Assess this cell for malaria.
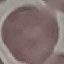

Uninfected.

Acquired by smartphone through the microscope eyepiece. Giemsa-stained preparation. Thin blood film. Cell patch, automatically extracted from a larger field of view and resized to 64 × 64 pixels.